Outline each blood parasite and name the species.
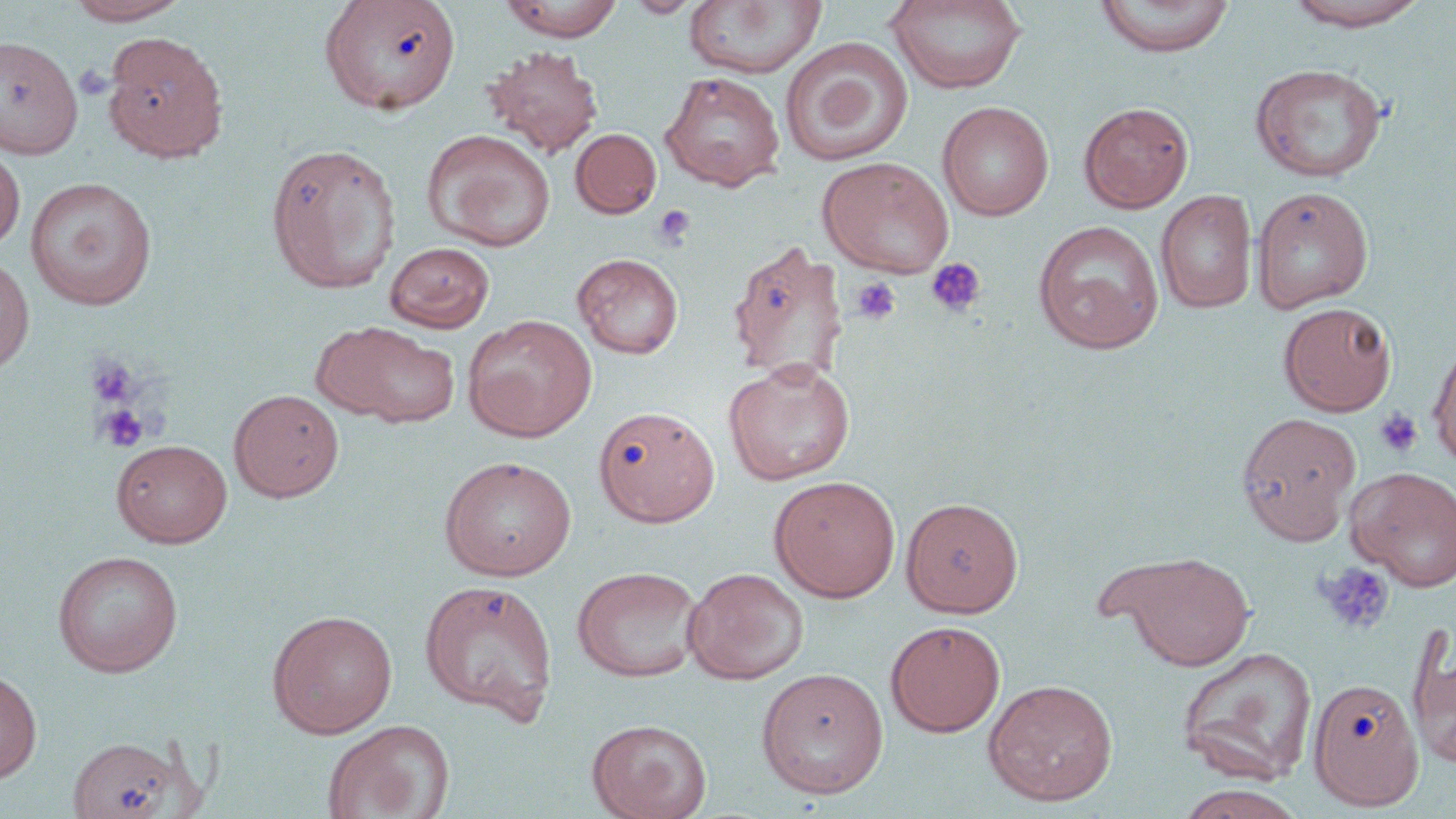
No blood parasites observed.

slide-level diagnosis = no evidence of blood parasites
preparation = thin blood smear
modality = light microscopy
image size = 1456×819 pixels
magnification = 1000x
field of view = one of a larger specimen
stain = May-Grünwald-Giemsa
platelet locations = approximate bounding boxes as named x1/y1/x2/y2 corners in pixels: (x1=653, y1=206, x2=696, y2=249), (x1=926, y1=257, x2=986, y2=316), (x1=852, y1=277, x2=900, y2=325), (x1=85, y1=356, x2=140, y2=408), (x1=95, y1=404, x2=149, y2=452), (x1=1375, y1=408, x2=1423, y2=458), (x1=1314, y1=562, x2=1395, y2=636)
uninfected red blood cell locations = approximate bounding boxes as named x1/y1/x2/y2 corners in pixels: (x1=64, y1=0, x2=192, y2=26), (x1=498, y1=0, x2=625, y2=41), (x1=625, y1=0, x2=702, y2=18), (x1=1094, y1=0, x2=1236, y2=58), (x1=319, y1=1, x2=462, y2=114), (x1=887, y1=1, x2=1027, y2=94), (x1=1285, y1=1, x2=1430, y2=32), (x1=684, y1=2, x2=827, y2=79), (x1=102, y1=31, x2=229, y2=162), (x1=0, y1=35, x2=83, y2=160), (x1=779, y1=36, x2=914, y2=166), (x1=483, y1=44, x2=604, y2=158), (x1=1249, y1=62, x2=1389, y2=182), (x1=659, y1=70, x2=786, y2=191), (x1=937, y1=100, x2=1055, y2=221), (x1=1079, y1=101, x2=1194, y2=213), (x1=570, y1=128, x2=662, y2=219), (x1=421, y1=129, x2=556, y2=251), (x1=0, y1=141, x2=25, y2=252), (x1=264, y1=142, x2=400, y2=293), (x1=817, y1=156, x2=954, y2=276), (x1=24, y1=176, x2=157, y2=310), (x1=1251, y1=186, x2=1375, y2=312), (x1=1155, y1=189, x2=1258, y2=314), (x1=1032, y1=220, x2=1164, y2=353), (x1=726, y1=240, x2=849, y2=386), (x1=384, y1=242, x2=495, y2=333), (x1=572, y1=253, x2=684, y2=359), (x1=0, y1=257, x2=35, y2=373), (x1=1278, y1=302, x2=1396, y2=416), (x1=462, y1=315, x2=597, y2=441), (x1=315, y1=321, x2=459, y2=428), (x1=1427, y1=341, x2=1456, y2=470), (x1=723, y1=358, x2=856, y2=486), (x1=229, y1=388, x2=344, y2=502), (x1=594, y1=405, x2=721, y2=527), (x1=1236, y1=411, x2=1361, y2=544), (x1=112, y1=439, x2=232, y2=547), (x1=438, y1=455, x2=577, y2=581), (x1=1345, y1=466, x2=1456, y2=592), (x1=768, y1=475, x2=901, y2=602), (x1=901, y1=497, x2=1023, y2=617), (x1=52, y1=550, x2=183, y2=677), (x1=1107, y1=550, x2=1256, y2=671), (x1=571, y1=565, x2=704, y2=682), (x1=683, y1=567, x2=809, y2=684), (x1=419, y1=579, x2=558, y2=724), (x1=266, y1=609, x2=398, y2=738), (x1=885, y1=620, x2=1005, y2=737), (x1=1408, y1=634, x2=1456, y2=772), (x1=1176, y1=646, x2=1318, y2=786), (x1=755, y1=667, x2=889, y2=800), (x1=0, y1=668, x2=42, y2=784), (x1=1308, y1=677, x2=1424, y2=810), (x1=982, y1=678, x2=1119, y2=806), (x1=586, y1=718, x2=712, y2=819), (x1=321, y1=719, x2=455, y2=819), (x1=67, y1=735, x2=186, y2=819), (x1=1174, y1=784, x2=1307, y2=819)